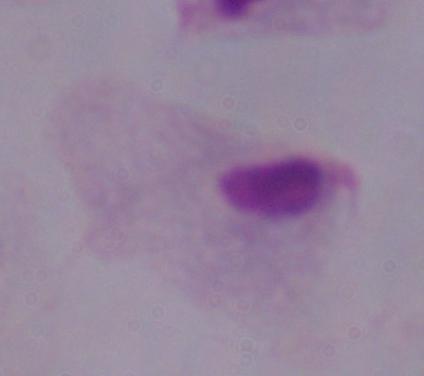 A trichomonad is seen. Photomicrograph. Captured at 1000x magnification.